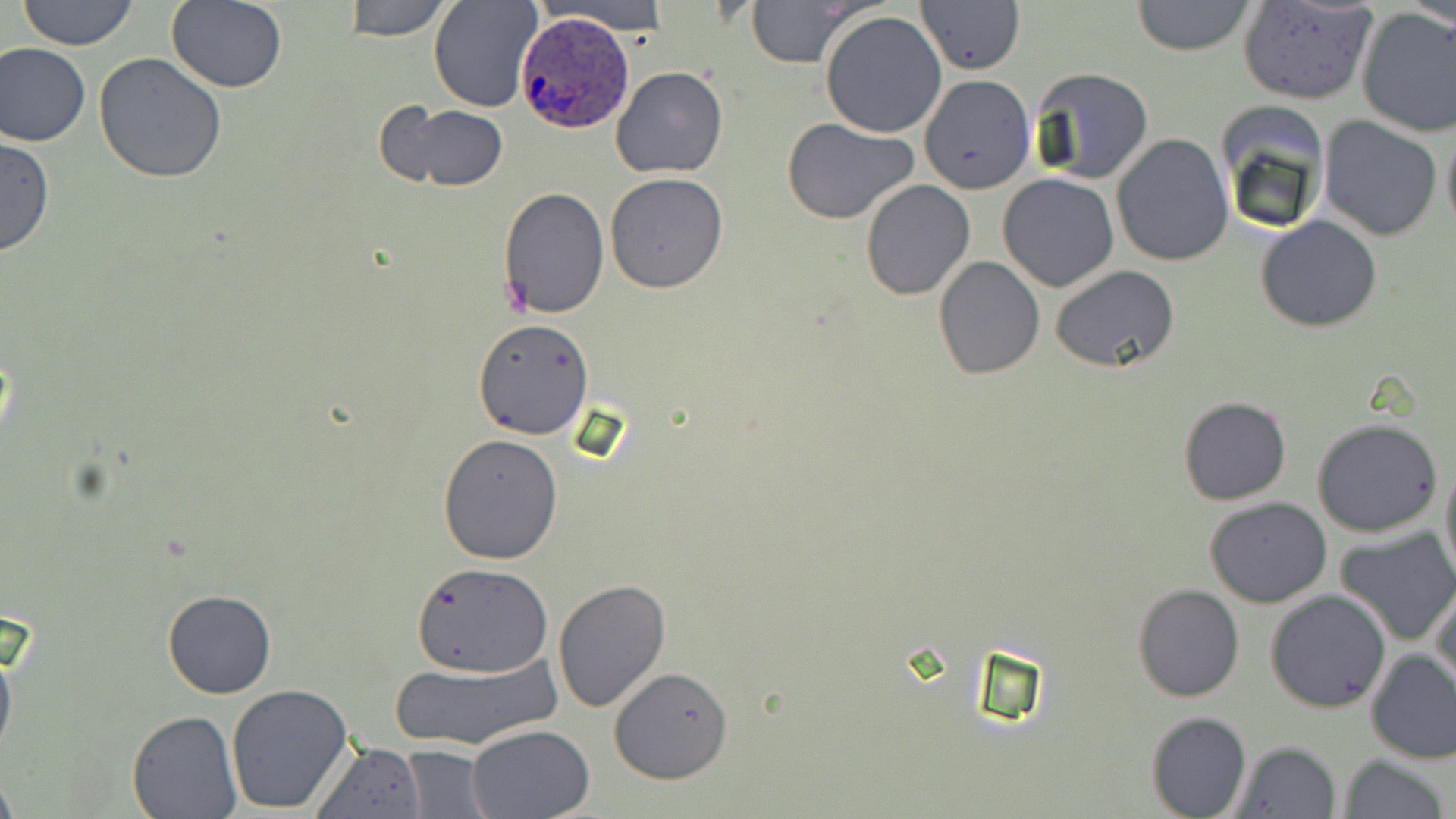

Summary:
  - Coordinate format: approximate bounding boxes as (x1, y1, x2, y2) in pixels
  - Plasmodium ovale-infected red blood cell locations: (514, 12, 633, 130)
  - Uninfected red blood cell locations: (17, 0, 140, 50), (343, 0, 452, 42), (427, 0, 542, 112), (535, 0, 679, 35), (744, 0, 865, 67), (1131, 0, 1258, 56), (1409, 0, 1455, 33), (917, 1, 1026, 73), (1236, 1, 1378, 105), (167, 2, 288, 94), (1355, 8, 1456, 139), (819, 10, 948, 139), (0, 42, 92, 148), (94, 52, 227, 183), (610, 65, 729, 180), (1028, 67, 1154, 185), (918, 73, 1036, 196), (390, 103, 508, 192), (1213, 106, 1328, 236), (1318, 115, 1443, 241), (783, 118, 917, 223), (1441, 120, 1456, 238), (1112, 134, 1232, 266), (0, 136, 55, 258), (605, 173, 729, 294), (998, 173, 1120, 292), (860, 180, 975, 300), (497, 186, 609, 318), (1256, 215, 1382, 332), (934, 255, 1044, 378), (1050, 267, 1180, 372), (473, 318, 595, 439), (1178, 395, 1292, 506), (1312, 418, 1443, 537), (437, 432, 564, 563), (1439, 449, 1456, 590), (1205, 496, 1332, 607), (1335, 527, 1456, 648), (413, 563, 550, 678), (552, 576, 672, 712), (1430, 580, 1456, 694), (1133, 584, 1244, 702), (161, 589, 276, 699), (1266, 589, 1392, 713), (0, 628, 18, 768), (1366, 649, 1456, 763), (391, 655, 562, 751), (609, 667, 734, 785), (224, 683, 353, 815), (128, 711, 242, 817), (1146, 712, 1251, 819), (465, 723, 595, 818), (1230, 740, 1342, 819), (312, 742, 427, 819), (400, 746, 491, 817), (1337, 755, 1449, 818), (0, 772, 19, 819)
  - Slide-level diagnosis: Plasmodium ovale
  - Image size: 1456×819 pixels
  - Field of view: single
  - Preparation: thin blood smear
  - Magnification: 1000x
  - Stain: May-Grünwald-Giemsa
  - Modality: light microscopy